Report the malaria status of this cell.
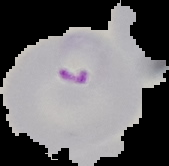
It is parasitized.

Summary:
  - Image size: 169×166 pixels
  - Image type: cell region segmented out of the field of view; surrounding area masked to black
  - Preparation: thin blood smear